Point out each Plasmodium parasite.
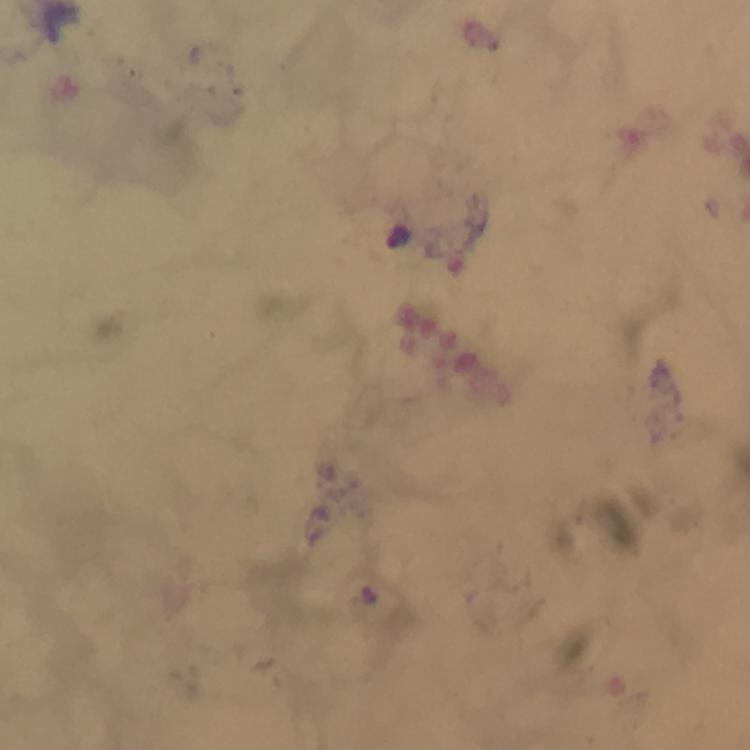
Approximate centers as (x, y) in pixels.
Plasmodium parasites: (367, 596).

Thick blood smear. At 100x magnification. From a malaria diagnostic workup. Giemsa stain. Immersion oil was used. Cropped region of a single field of view. Image is 750×750 pixels. Photographed with a smartphone mounted on the microscope.